Give the position of every P. falciparum parasite, noting its life-cycle stage.
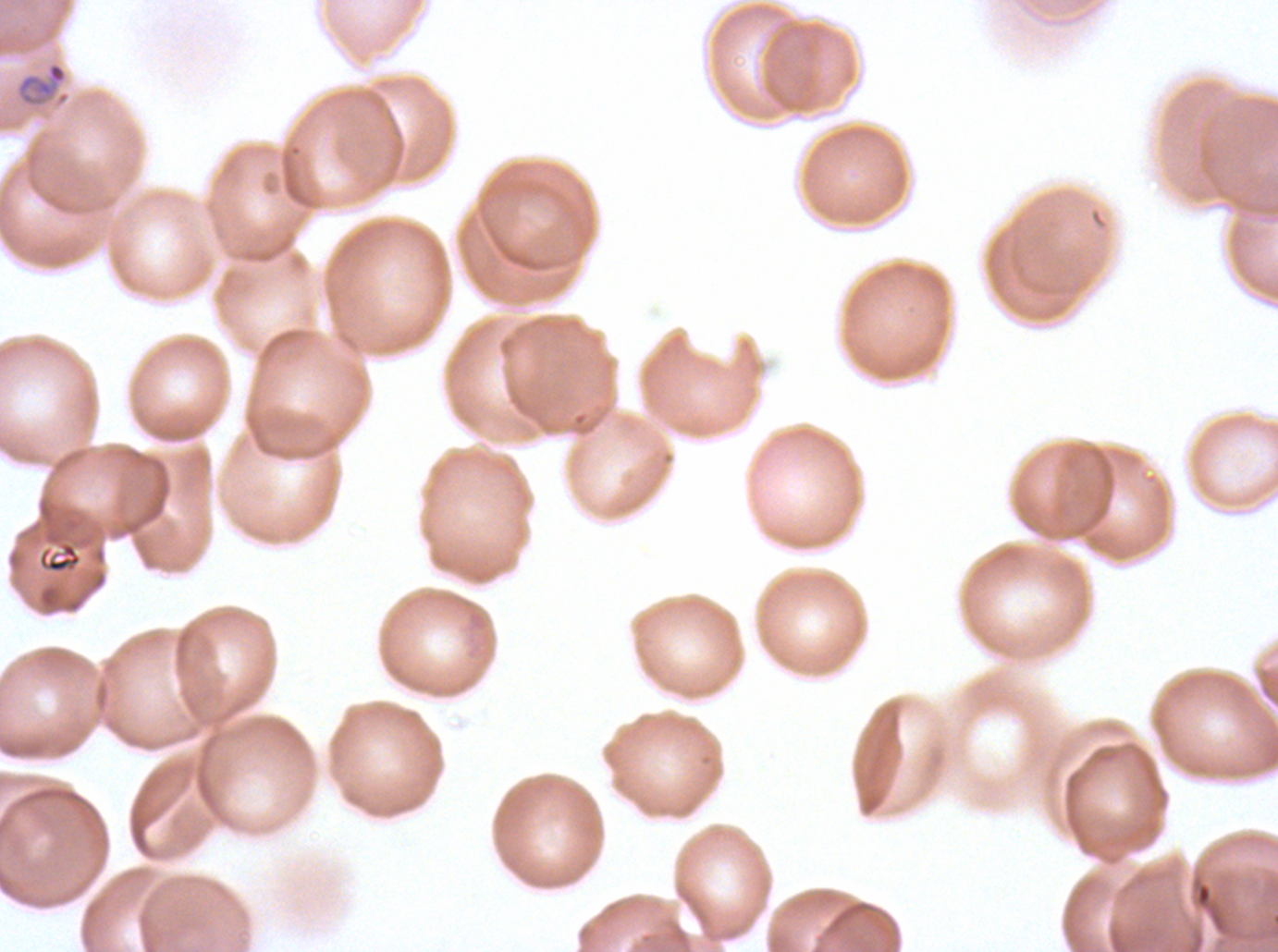

Approximate bounding rectangles given as corner coordinates in pixels from the top-left.
Rings: (x1=15, y1=61, x2=70, y2=108).
No late-ring/early-trophozoite forms, mid trophozoites, late trophozoites, early schizonts, late schizonts, segmenters, or gametocytes observed.

Summary:
  - Debris locations: (x1=38, y1=542, x2=82, y2=573)
  - Preparation: thin blood film
  - Specimen: ex-vivo P. falciparum culture from a patient in The Gambia, grown for 24 to 48 hours
  - Stain: Giemsa
  - Image size: 1278×952 pixels
  - Field of view: sub-image separated from a larger composite